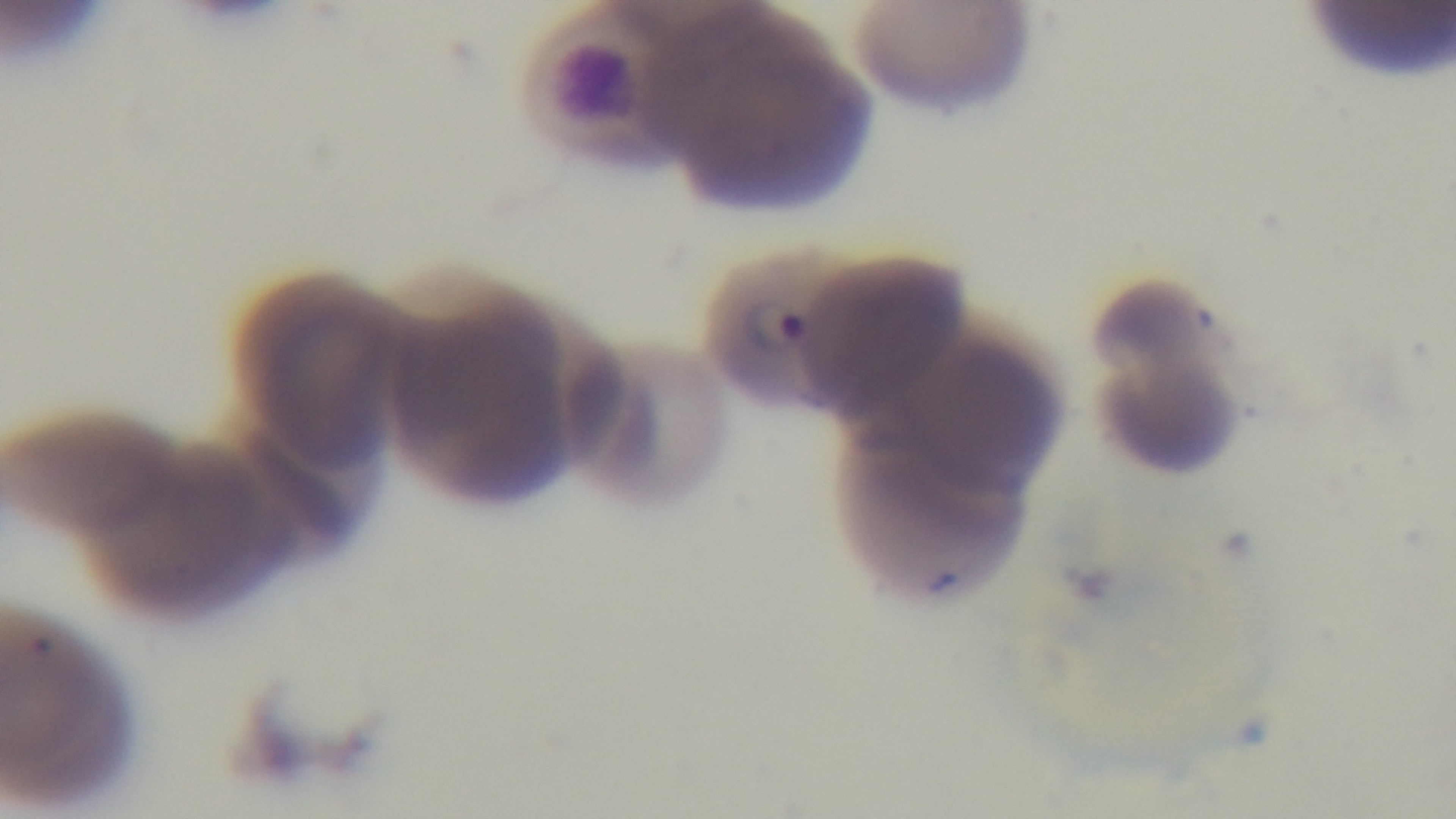
Summary:
  - Stain: Giemsa
  - Field of view: single
  - Malaria status: positive
  - Objective: 100x oil immersion
  - Capture: mounted 4K digital camera
  - Modality: light microscopy
  - Preparation: thin smear